Comment on the morphology of the red blood cells.
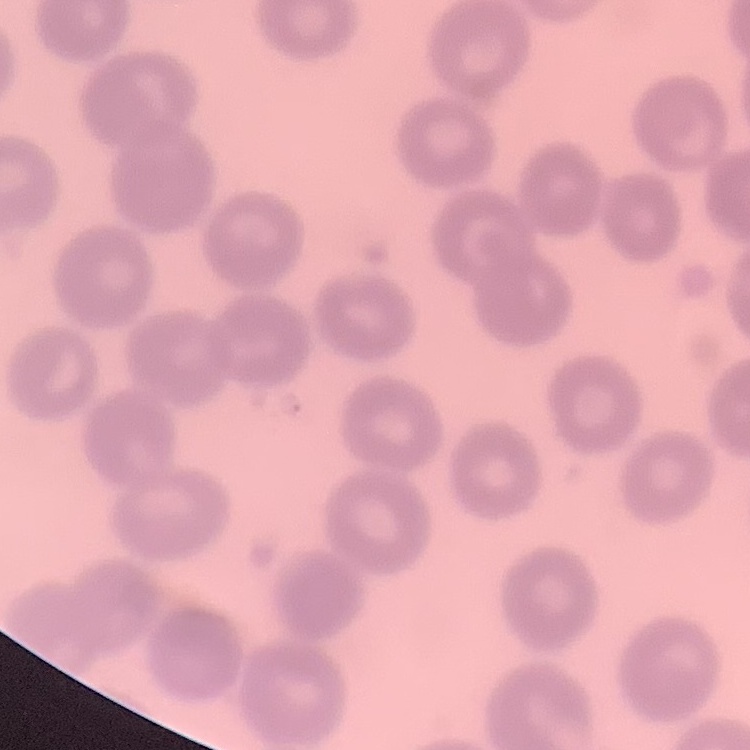

No rouleaux formation.

stain = Field's or Giemsa
image type = square crop of a larger photomicrograph
preparation = thin blood smear